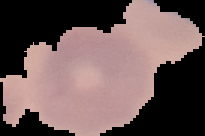
{
  "preparation": "thin blood smear",
  "image_type": "cell region segmented out of the field of view; surrounding area masked to black",
  "image_size": "205×136 pixels",
  "malaria_status": "uninfected"
}